Describe the morphology of the red blood cells.
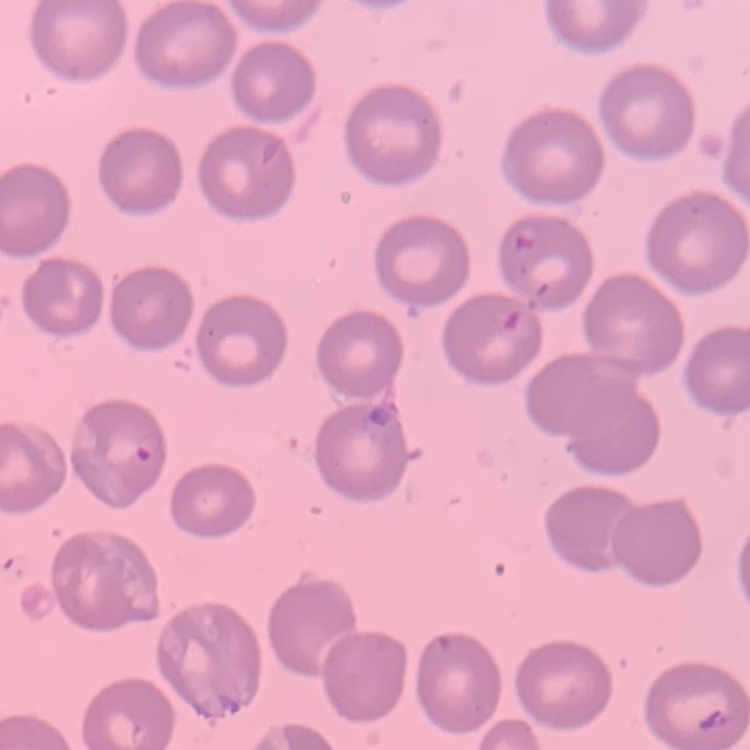

They show no rouleaux formation.

Summary:
  - Stain: Field's or Giemsa
  - Image type: one tile cut from a larger photomicrograph
  - Preparation: thin blood smear